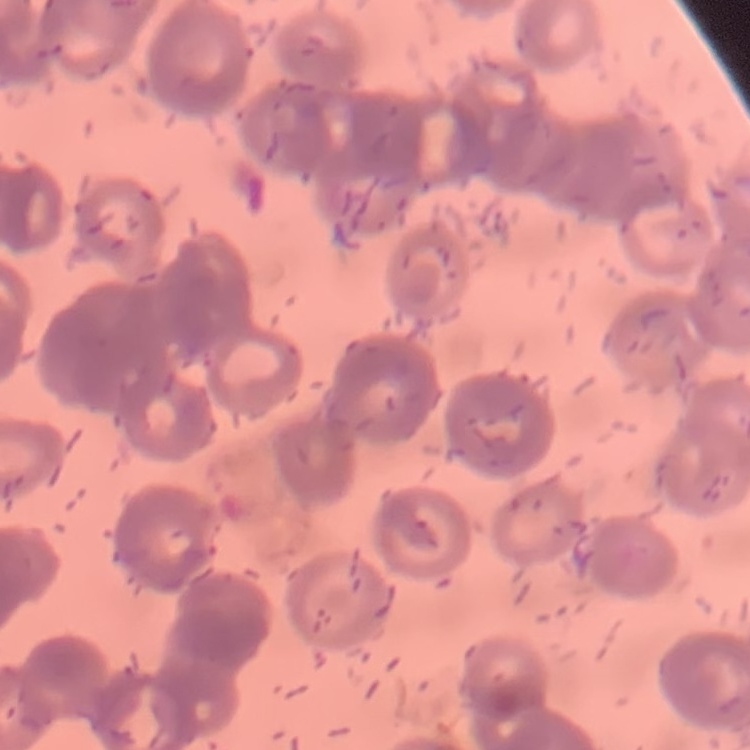

erythrocyte morphology = rouleaux formation
stain = Field's or Giemsa
preparation = thin blood smear
image type = square crop of a larger photomicrograph